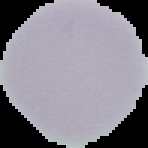 Result: negative for Plasmodium parasites. Image is 148×148 pixels. From a thin blood film. Cell region segmented out of the field of view; the surrounding area is masked to black.